Report the malaria status of this cell.
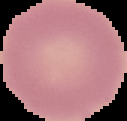

It is uninfected.

Summary:
  - Preparation: thin blood smear
  - Image type: segmented cell region with the area outside set to black
  - Image size: 127×121 pixels